State which cell type is depicted.
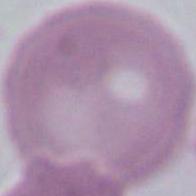

This is an erythrocyte.

Captured at 1000x magnification. Micrograph.